Name the cell type shown.
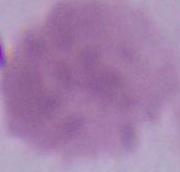

This is an erythrocyte.

Summary:
  - Magnification: 1000x
  - Modality: micrograph